Give a bounding box for every malaria parasite.
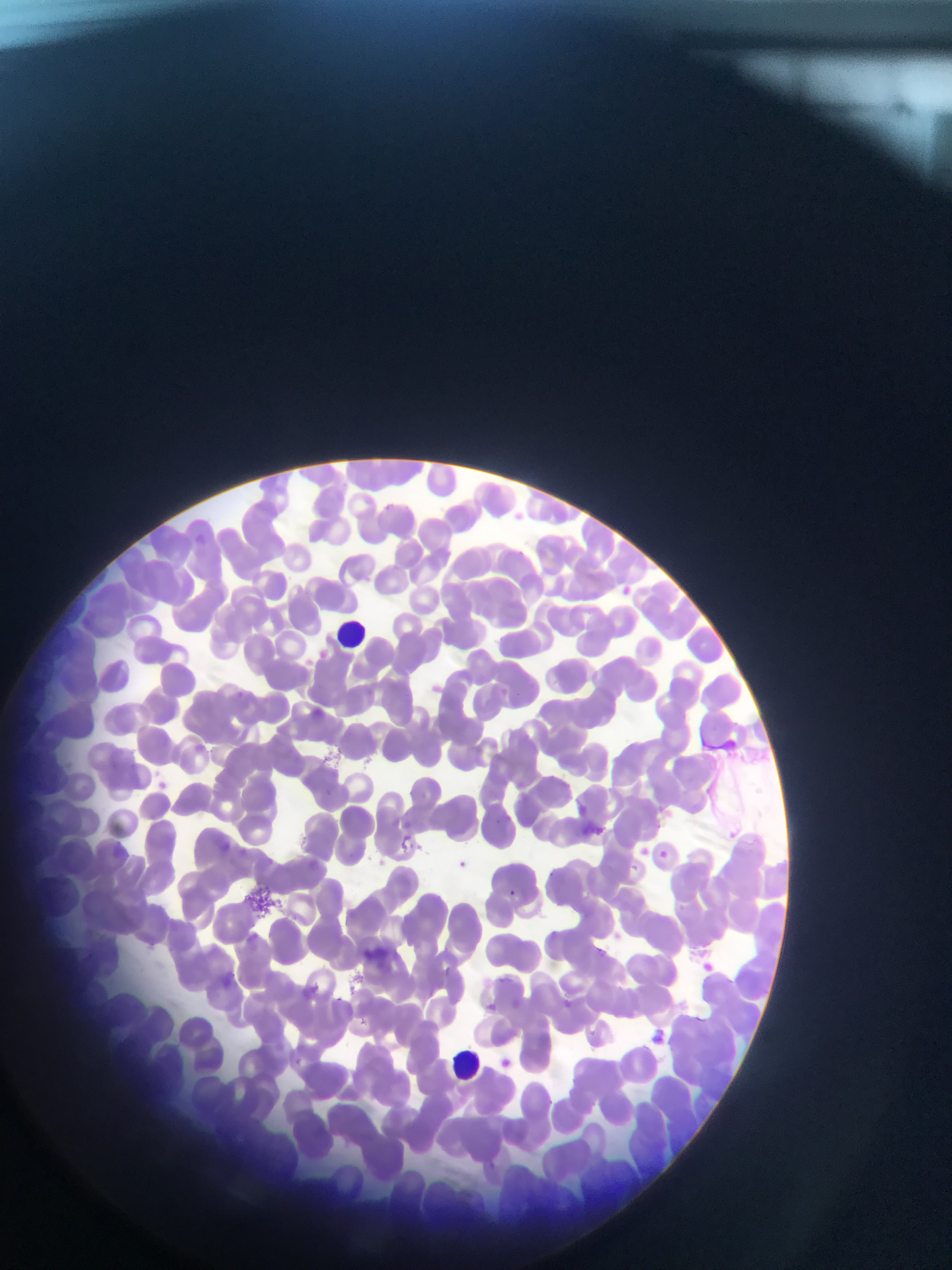

Approximate bounding boxes as left top right bottom in pixels.
Malaria parasites: 617 583 635 600; 317 647 330 660; 232 687 248 701; 307 706 327 722; 389 815 406 829; 591 825 608 839; 397 835 421 856; 215 840 234 857; 407 840 425 855; 657 848 672 862; 453 857 470 872; 628 862 647 878; 545 869 567 884; 504 888 519 903; 598 943 615 958; 697 960 716 976; 568 993 583 1004; 483 1000 499 1015; 589 1023 606 1044; 288 1054 306 1072; 496 1056 515 1073.

Summary:
  - Leukocyte locations: 334 616 375 648; 441 1048 482 1078
  - Artifact (stain precipitate or debris) locations: 242 876 272 920
  - Field of view: single
  - Country: Ghana
  - Preparation: thin blood smear
  - Capture: mobile-phone photograph through a microscope
  - Image size: 952×1270 pixels